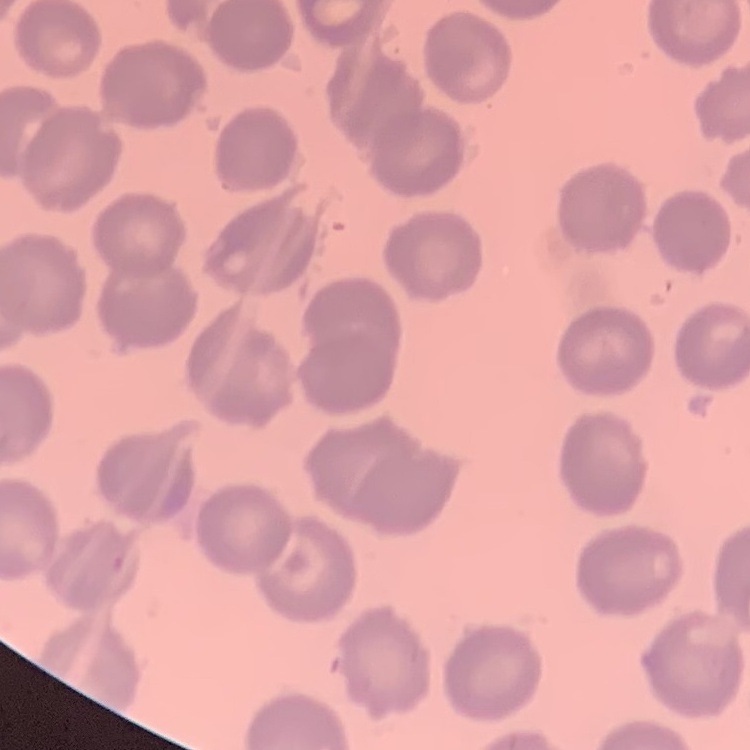
red blood cell morphology = no rouleaux formation
image type = one tile cut from a larger photomicrograph
stain = Field's or Giemsa
preparation = thin blood film